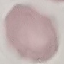

Malaria status: uninfected. Cell patch, automatically extracted from a larger field of view and resized to 64 × 64 pixels. Giemsa-stained preparation. Thin smear of blood. Acquired by smartphone through the microscope eyepiece.